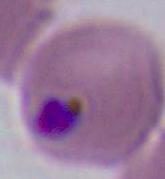
{
  "identification": "Plasmodium",
  "magnification": "400x or 1000x",
  "modality": "photomicrograph"
}